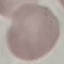 Result: no malaria parasites detected. Thin smear of blood. Cell patch, automatically extracted from a larger field of view and resized to 64 × 64 pixels. Giemsa-stained preparation. Photographed with a smartphone camera at the microscope eyepiece.